Outline each blood parasite and name the species.
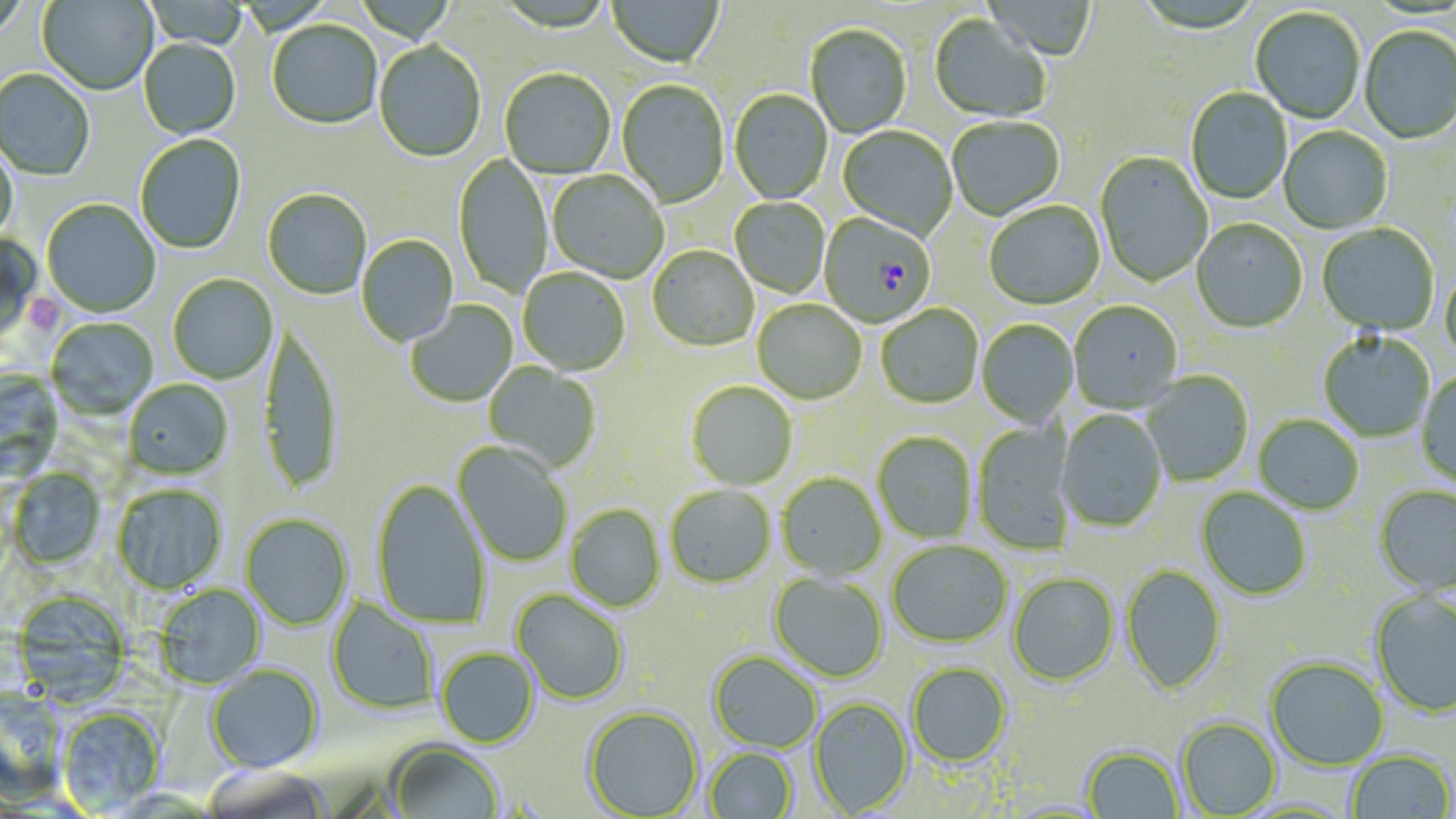
Approximate bounding boxes as named x1/y1/x2/y2 corners in pixels.
Plasmodium falciparum-infected red blood cells: (x1=822, y1=214, x2=933, y2=328).
No Plasmodium ovale, Plasmodium malariae, Plasmodium vivax, Babesia divergens, or Trypanosoma brucei observed.

Platelet locations: (x1=20, y1=292, x2=63, y2=336). Uninfected red blood cell locations: (x1=0, y1=0, x2=29, y2=43), (x1=38, y1=0, x2=159, y2=97), (x1=142, y1=1, x2=249, y2=49), (x1=607, y1=1, x2=723, y2=70), (x1=984, y1=1, x2=1097, y2=62), (x1=1250, y1=8, x2=1365, y2=125), (x1=929, y1=16, x2=1051, y2=124), (x1=267, y1=22, x2=382, y2=130), (x1=805, y1=25, x2=912, y2=139), (x1=1358, y1=27, x2=1456, y2=145), (x1=139, y1=39, x2=241, y2=140), (x1=373, y1=43, x2=486, y2=163), (x1=0, y1=69, x2=95, y2=182), (x1=500, y1=70, x2=616, y2=180), (x1=617, y1=81, x2=729, y2=209), (x1=1185, y1=88, x2=1292, y2=205), (x1=729, y1=91, x2=832, y2=205), (x1=947, y1=117, x2=1066, y2=221), (x1=838, y1=127, x2=957, y2=241), (x1=1279, y1=127, x2=1393, y2=234), (x1=135, y1=134, x2=246, y2=255), (x1=0, y1=140, x2=19, y2=245), (x1=1094, y1=152, x2=1212, y2=288), (x1=453, y1=154, x2=552, y2=299), (x1=548, y1=171, x2=668, y2=283), (x1=262, y1=190, x2=372, y2=300), (x1=730, y1=198, x2=830, y2=298), (x1=41, y1=200, x2=161, y2=318), (x1=984, y1=203, x2=1105, y2=311), (x1=1191, y1=220, x2=1307, y2=334), (x1=1316, y1=224, x2=1439, y2=336), (x1=0, y1=231, x2=41, y2=343), (x1=356, y1=235, x2=459, y2=347), (x1=647, y1=246, x2=758, y2=352), (x1=1440, y1=266, x2=1456, y2=369), (x1=518, y1=268, x2=630, y2=376), (x1=168, y1=275, x2=278, y2=384), (x1=406, y1=300, x2=518, y2=408), (x1=752, y1=300, x2=866, y2=405), (x1=1069, y1=303, x2=1183, y2=415), (x1=876, y1=305, x2=983, y2=409), (x1=47, y1=318, x2=158, y2=422), (x1=977, y1=320, x2=1079, y2=428), (x1=258, y1=328, x2=343, y2=494), (x1=1318, y1=332, x2=1435, y2=442), (x1=483, y1=361, x2=601, y2=472), (x1=0, y1=370, x2=64, y2=486), (x1=1416, y1=370, x2=1456, y2=489), (x1=1143, y1=372, x2=1254, y2=487), (x1=124, y1=380, x2=234, y2=481), (x1=686, y1=382, x2=797, y2=491), (x1=1056, y1=410, x2=1167, y2=532), (x1=1253, y1=415, x2=1364, y2=515), (x1=972, y1=420, x2=1078, y2=555), (x1=872, y1=432, x2=977, y2=543), (x1=452, y1=442, x2=572, y2=567), (x1=7, y1=468, x2=106, y2=571), (x1=776, y1=473, x2=887, y2=582), (x1=371, y1=480, x2=491, y2=629), (x1=112, y1=485, x2=227, y2=595), (x1=1374, y1=485, x2=1456, y2=596), (x1=665, y1=486, x2=776, y2=589), (x1=1196, y1=488, x2=1312, y2=601), (x1=566, y1=505, x2=665, y2=612), (x1=240, y1=514, x2=353, y2=631), (x1=887, y1=540, x2=1012, y2=648), (x1=1120, y1=564, x2=1226, y2=696), (x1=769, y1=573, x2=888, y2=683), (x1=1007, y1=573, x2=1119, y2=687), (x1=154, y1=584, x2=266, y2=690), (x1=511, y1=590, x2=629, y2=706), (x1=12, y1=591, x2=132, y2=707), (x1=1369, y1=591, x2=1456, y2=717), (x1=326, y1=597, x2=439, y2=716), (x1=435, y1=649, x2=538, y2=749), (x1=707, y1=652, x2=822, y2=753), (x1=1265, y1=657, x2=1389, y2=770), (x1=906, y1=662, x2=1011, y2=767), (x1=206, y1=664, x2=324, y2=774), (x1=1, y1=692, x2=67, y2=804), (x1=808, y1=697, x2=913, y2=817), (x1=582, y1=707, x2=703, y2=818), (x1=57, y1=708, x2=165, y2=815), (x1=1176, y1=718, x2=1281, y2=817), (x1=386, y1=741, x2=504, y2=819), (x1=1081, y1=746, x2=1184, y2=818), (x1=704, y1=747, x2=798, y2=818), (x1=1345, y1=751, x2=1454, y2=818), (x1=201, y1=766, x2=332, y2=819). Slide-level diagnosis: Plasmodium falciparum. May-Grünwald-Giemsa stain. Image is 1456×819 pixels. Optical microscopy. 1000x magnification. Thin blood smear. Single field of view.